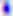

magnification = 400x
identification = Toxoplasma gondii
modality = micrograph